Point out each Plasmodium parasite.
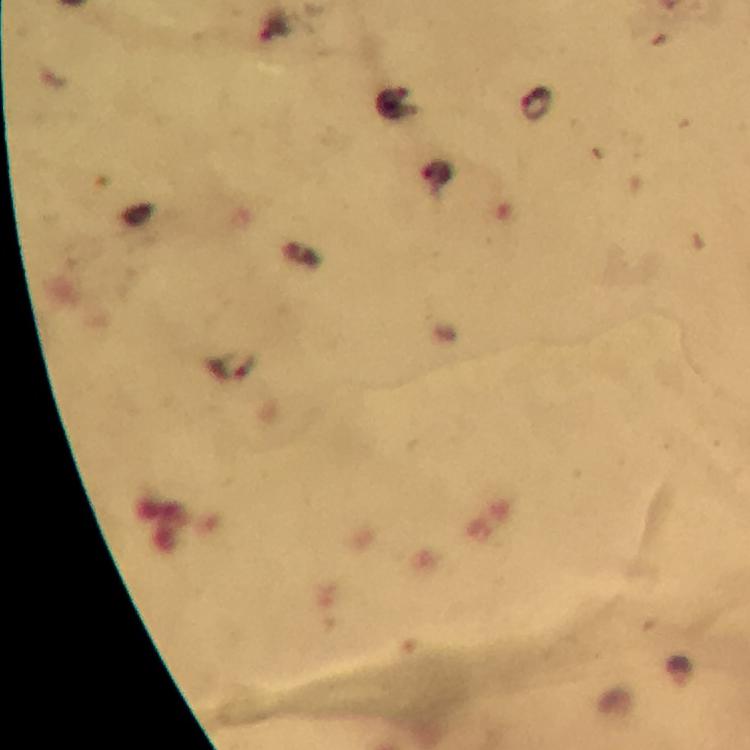

Approximate centers as {x, y} in pixels.
Plasmodium parasites: {536, 104}.

{
  "cropped_from": "one field of view",
  "context": "from a malaria diagnostic workup",
  "magnification": "100x",
  "image_size": "750×750 pixels",
  "stain": "Giemsa",
  "capture": "smartphone mounted on the microscope",
  "preparation": "thick smear",
  "immersion_oil": "applied"
}